Comment on the morphology of the erythrocytes.
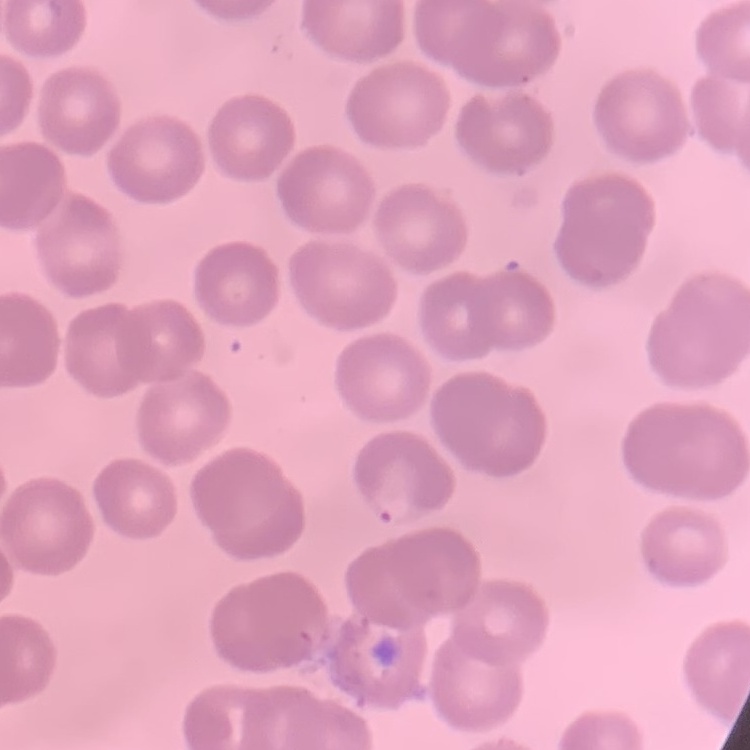

They show no rouleaux formation.

Summary:
  - Image type: square crop of a larger photomicrograph
  - Preparation: thin blood smear
  - Stain: Field's or Giemsa